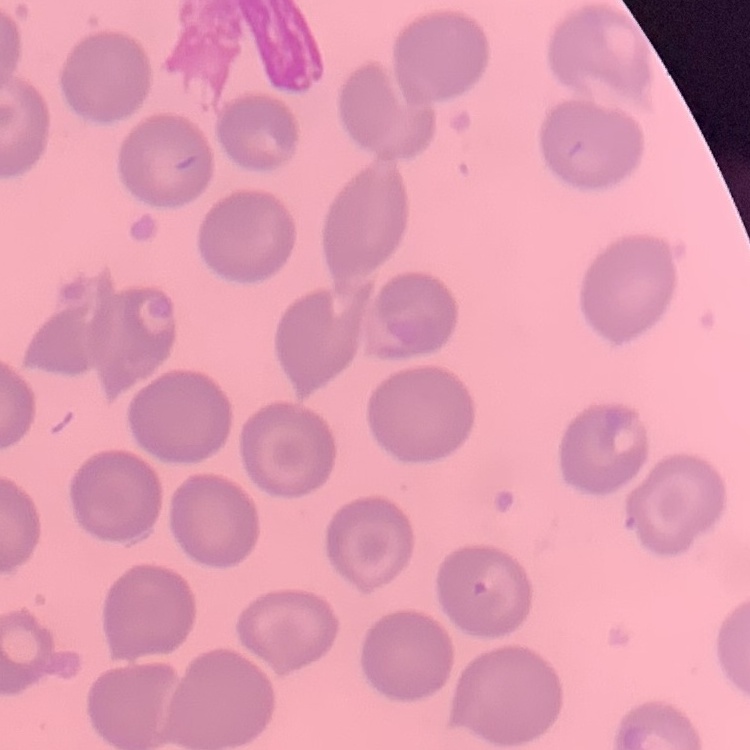 The erythrocytes exhibit no rouleaux formation. Stained with either Field's or Giemsa. Square crop of a larger photomicrograph. Thin blood smear.